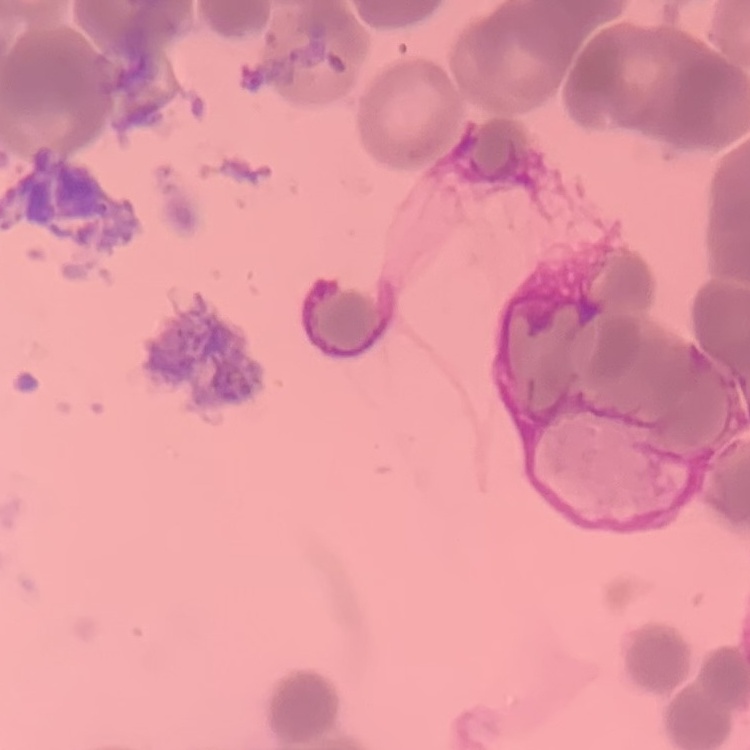

red blood cell morphology = rouleaux formation
preparation = thin blood film
stain = Field's or Giemsa
image type = square crop of a larger photomicrograph